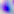
Summary:
  - Magnification: 400x
  - Modality: micrograph
  - Identification: Toxoplasma gondii